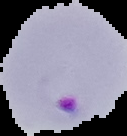
Summary:
  - Image size: 127×136 pixels
  - Malaria status: parasitized
  - Image type: segmented cell region on a black background
  - Preparation: thin blood smear